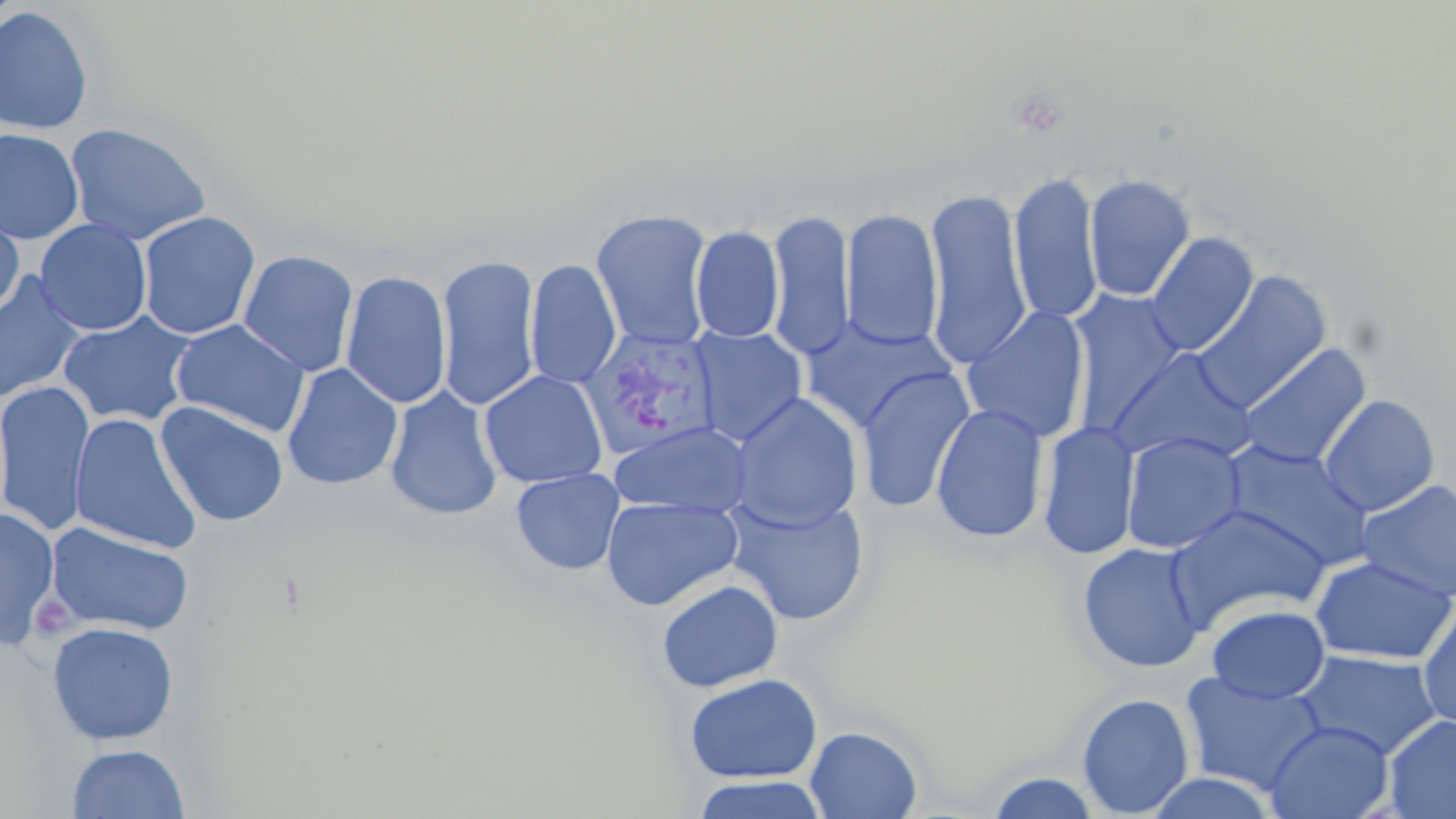

slide-level diagnosis = Plasmodium vivax
preparation = thin blood film
field of view = one of a larger specimen
uninfected red blood cell locations = approximate bounding boxes as (x1,y1)-(x2,y2) corner pairs in pixels: (0,6)-(94,135), (64,122)-(213,246), (0,128)-(84,245), (1007,170)-(1105,327), (1083,172)-(1197,302), (922,185)-(1033,367), (840,206)-(945,352), (590,207)-(716,350), (0,208)-(25,320), (765,208)-(856,362), (136,210)-(262,340), (34,218)-(153,336), (690,224)-(785,344), (1145,231)-(1260,357), (237,249)-(360,377), (435,254)-(542,412), (525,258)-(622,389), (339,269)-(453,410), (1190,269)-(1333,412), (0,272)-(88,406), (1065,292)-(1190,430), (959,304)-(1092,444), (57,310)-(198,429), (800,316)-(959,432), (170,319)-(311,437), (690,326)-(808,445), (1236,342)-(1372,470), (1107,346)-(1260,467), (282,362)-(403,490), (855,365)-(976,513), (478,369)-(609,489), (0,379)-(95,539), (384,385)-(504,520), (728,392)-(863,532), (1318,393)-(1440,517), (154,401)-(289,527), (930,402)-(1050,544), (69,412)-(202,555), (1037,419)-(1141,560), (609,420)-(755,516), (1121,431)-(1247,554), (1219,439)-(1375,569), (510,467)-(625,575), (1355,479)-(1456,604), (724,494)-(870,626), (600,495)-(743,611), (0,505)-(60,649), (1167,505)-(1331,627), (44,521)-(195,638), (1077,541)-(1207,674), (1309,554)-(1455,665), (657,579)-(784,693), (1417,603)-(1456,732), (1206,604)-(1330,704), (46,621)-(179,746), (1292,649)-(1443,759), (1179,669)-(1328,795), (684,672)-(823,784), (1076,693)-(1195,817), (1383,713)-(1456,819), (1262,719)-(1395,819), (805,725)-(923,818), (66,743)-(190,818), (983,771)-(1104,818), (1140,771)-(1279,817), (691,774)-(828,818)
stain = May-Grünwald-Giemsa
image size = 1456×819 pixels
modality = optical microscopy
magnification = 1000x
Plasmodium vivax-infected red blood cell locations = approximate bounding boxes as (x1,y1)-(x2,y2) corner pairs in pixels: (581,327)-(723,459)